Name the parasite shown.
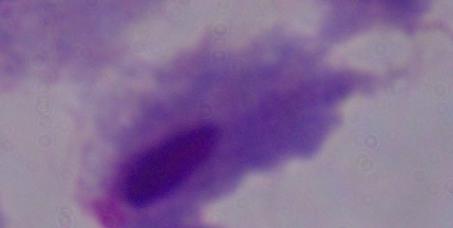

A trichomonad.

Summary:
  - Modality: micrograph
  - Magnification: 1000x